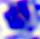
Summary:
  - Modality: micrograph
  - Identification: white blood cell
  - Magnification: 400x